Outline each blood parasite and name the species.
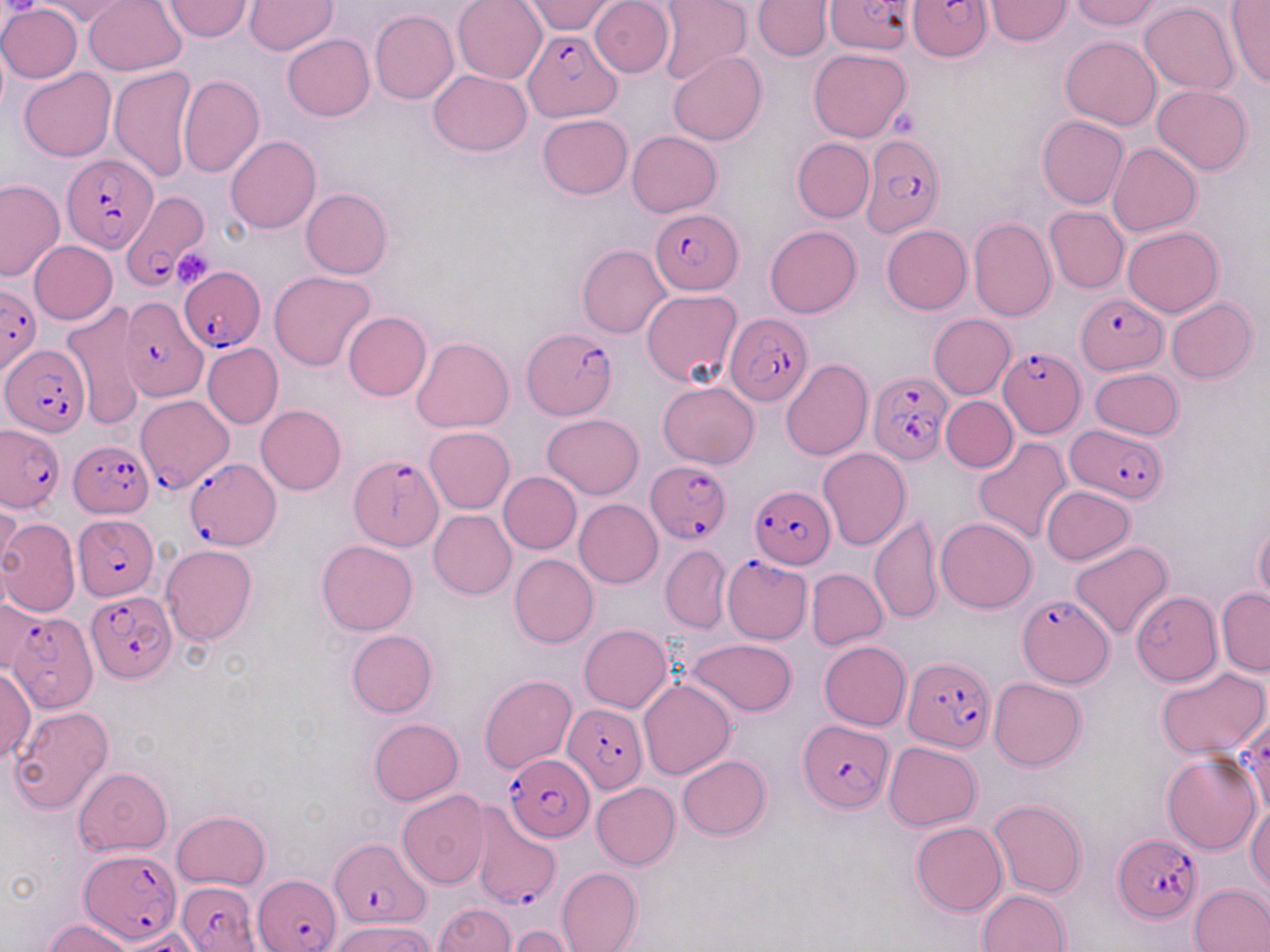
Approximate bounding boxes as [x1, y1, x2, y2] in pixels.
Plasmodium falciparum-infected red blood cells: [826, 0, 908, 51], [907, 0, 991, 62], [522, 31, 623, 121], [860, 133, 946, 238], [62, 155, 159, 253], [119, 194, 210, 294], [650, 208, 740, 292], [178, 266, 264, 350], [0, 282, 42, 378], [1075, 293, 1167, 373], [121, 295, 208, 400], [725, 313, 812, 408], [522, 328, 615, 418], [2, 347, 86, 435], [999, 350, 1085, 438], [868, 373, 953, 465], [129, 394, 228, 490], [0, 422, 66, 511], [1070, 426, 1166, 504], [68, 441, 154, 518], [185, 452, 279, 548], [348, 455, 444, 550], [646, 459, 730, 543], [748, 487, 832, 569], [75, 516, 156, 599], [86, 592, 177, 684], [1016, 594, 1113, 689], [11, 611, 97, 711], [903, 655, 996, 752], [563, 705, 647, 793], [798, 721, 891, 813], [505, 754, 595, 842], [468, 798, 564, 907], [1114, 833, 1202, 924], [329, 838, 427, 929], [81, 848, 181, 945], [255, 873, 341, 952], [177, 878, 262, 952].
No Plasmodium ovale, Plasmodium malariae, Plasmodium vivax, Babesia divergens, or Trypanosoma brucei observed.

Summary:
  - Uninfected red blood cell locations: [84, 0, 187, 75], [164, 0, 254, 41], [453, 0, 548, 84], [522, 0, 621, 35], [590, 0, 675, 78], [657, 0, 751, 87], [752, 0, 831, 61], [985, 0, 1071, 45], [1068, 0, 1164, 29], [245, 1, 336, 55], [1225, 1, 1270, 87], [37, 2, 133, 25], [1141, 2, 1238, 94], [0, 3, 82, 83], [368, 6, 545, 93], [369, 11, 459, 105], [283, 34, 375, 121], [1060, 35, 1161, 130], [809, 48, 912, 140], [668, 52, 766, 146], [109, 65, 195, 182], [19, 69, 115, 161], [428, 70, 530, 156], [176, 75, 264, 180], [1151, 85, 1253, 175], [537, 114, 632, 199], [1036, 115, 1129, 210], [626, 131, 722, 217], [226, 136, 321, 233], [792, 138, 874, 222], [1106, 142, 1202, 236], [0, 179, 67, 282], [300, 188, 392, 279], [1044, 207, 1129, 293], [968, 217, 1055, 321], [881, 224, 971, 313], [765, 225, 861, 318], [1122, 226, 1221, 317], [29, 240, 118, 324], [577, 244, 671, 338], [269, 270, 376, 371], [642, 289, 743, 387], [1165, 298, 1257, 383], [63, 304, 146, 431], [487, 309, 576, 400], [928, 314, 1016, 399], [412, 336, 514, 433], [202, 342, 283, 430], [780, 358, 873, 461], [1089, 368, 1185, 440], [658, 381, 759, 467], [941, 396, 1018, 472], [256, 404, 347, 494], [543, 413, 644, 498], [424, 427, 515, 513], [973, 437, 1073, 543], [818, 447, 911, 549], [498, 471, 582, 554], [1040, 485, 1134, 565], [0, 496, 22, 576], [574, 499, 664, 588], [429, 510, 517, 600], [869, 514, 941, 625], [0, 518, 80, 616], [935, 519, 1037, 614], [1254, 521, 1270, 609], [316, 540, 418, 636], [1069, 542, 1173, 640], [161, 544, 258, 646], [661, 545, 731, 633], [509, 554, 598, 647], [722, 556, 812, 644], [806, 567, 887, 649], [1216, 589, 1270, 675], [1131, 590, 1222, 686], [0, 599, 44, 676], [579, 623, 671, 714], [346, 629, 438, 718], [686, 638, 797, 717], [819, 641, 910, 731], [0, 666, 36, 765], [1155, 669, 1268, 759], [480, 675, 577, 774], [989, 677, 1086, 771], [638, 679, 735, 780], [10, 706, 114, 814], [1239, 712, 1270, 819], [369, 717, 463, 803], [884, 742, 981, 830], [1161, 753, 1261, 855], [678, 755, 771, 839], [73, 768, 172, 854], [592, 782, 680, 870], [397, 790, 489, 888], [989, 798, 1087, 899], [1247, 804, 1270, 892], [171, 810, 270, 890], [910, 822, 1008, 916], [556, 867, 642, 952], [1189, 884, 1270, 952], [977, 890, 1070, 952], [432, 904, 514, 952], [44, 919, 136, 952], [333, 920, 435, 952], [508, 926, 577, 951], [121, 929, 201, 951]
  - Platelet locations: [3, 0, 38, 18], [892, 110, 918, 138], [173, 248, 215, 291]
  - Slide-level diagnosis: Plasmodium falciparum
  - Magnification: 1000x
  - Modality: optical microscopy
  - Stain: May-Grünwald-Giemsa
  - Preparation: thin blood film
  - Image size: 1270×952 pixels
  - Field of view: one of a larger specimen